Assess the morphology of the erythrocytes.
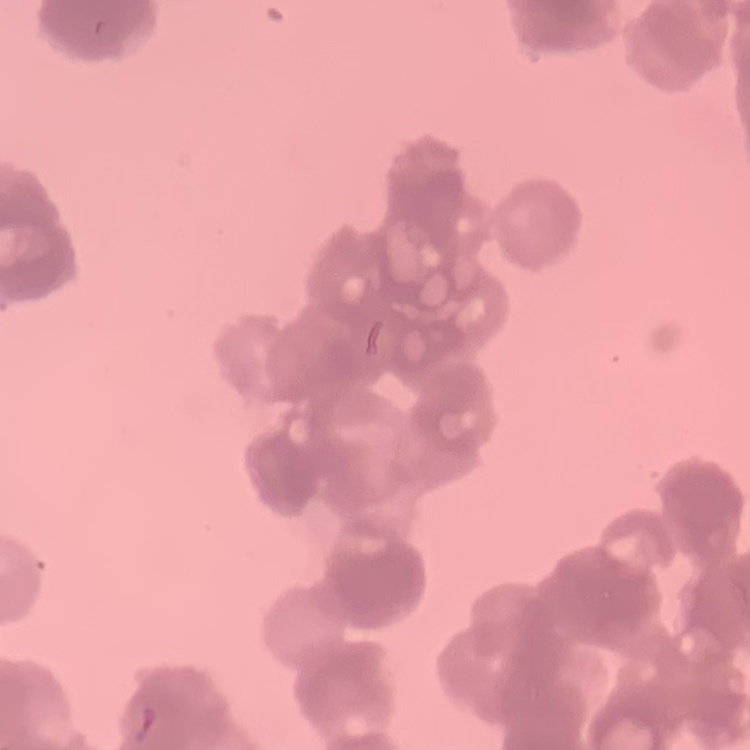

They show rouleaux formation.

stain = Field's or Giemsa
image type = one tile cut from a larger photomicrograph
preparation = thin blood film